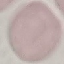

Summary:
  - Result: negative for malaria parasites
  - Stain: Giemsa
  - Capture: smartphone camera at the microscope eyepiece
  - Preparation: thin blood smear
  - Image type: automatically extracted cell patch, resized to 64 × 64 pixels